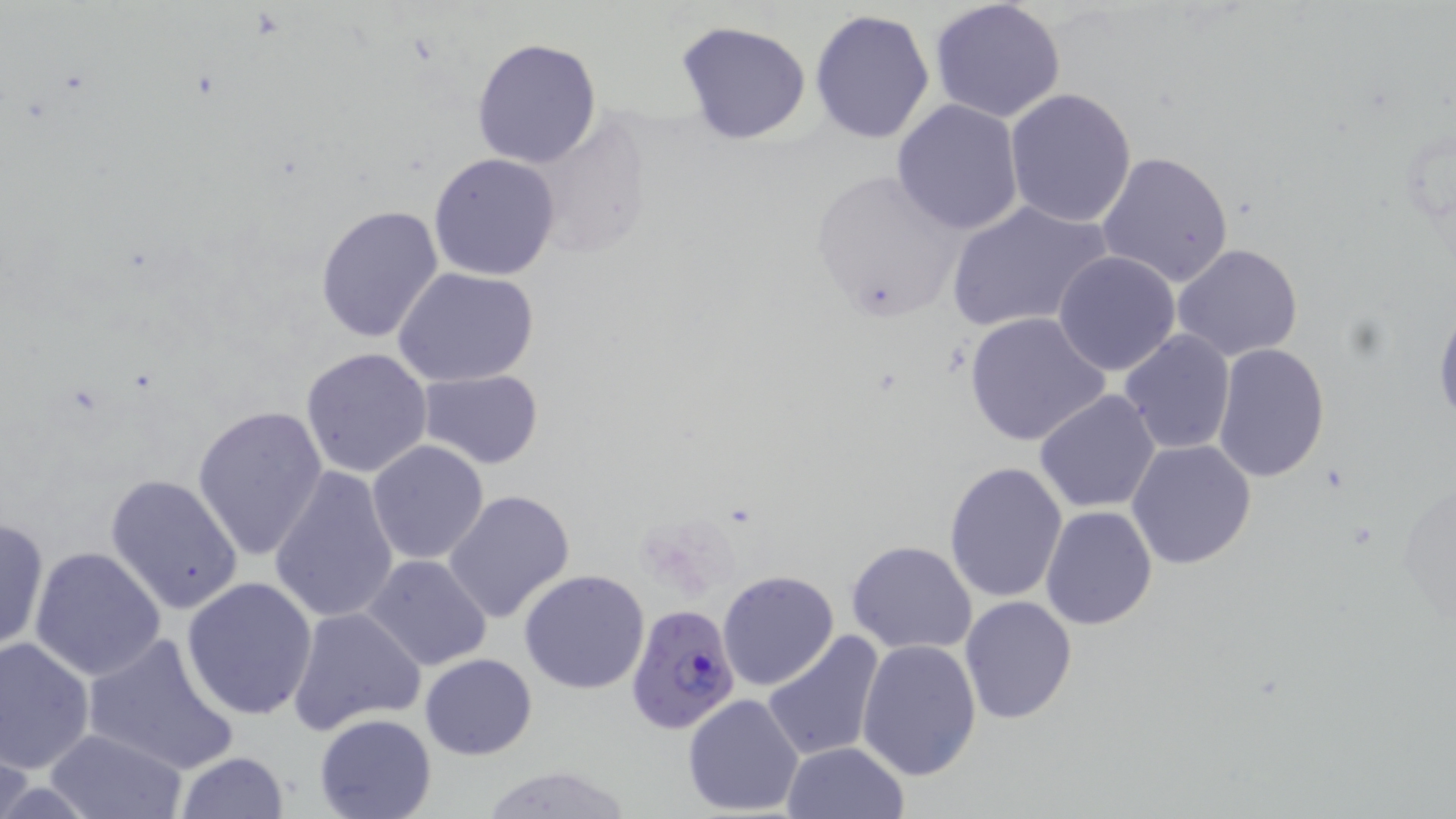 Approximate bounding boxes as (x1,y1)-(x2,y2) corner pairs in pixels. Uninfected red blood cell locations: (929,0)-(1067,123), (808,8)-(936,145), (676,20)-(812,145), (471,38)-(603,168), (1004,89)-(1137,227), (892,99)-(1024,234), (1097,151)-(1237,288), (429,152)-(562,281), (809,166)-(966,320), (946,198)-(1113,335), (315,203)-(444,344), (1172,244)-(1305,363), (1052,251)-(1180,376), (394,267)-(540,387), (1434,299)-(1456,429), (963,311)-(1111,448), (1117,331)-(1235,457), (1211,343)-(1329,484), (301,348)-(433,478), (417,369)-(545,470), (1034,389)-(1162,513), (191,405)-(328,560), (1127,440)-(1257,570), (367,441)-(490,566), (944,461)-(1069,602), (269,465)-(401,627), (105,473)-(244,615), (442,489)-(576,624), (1041,506)-(1157,629), (0,516)-(50,654), (846,539)-(979,655), (29,547)-(167,682), (363,554)-(494,672), (519,569)-(651,694), (719,570)-(838,691), (181,577)-(318,720), (958,594)-(1078,725), (287,607)-(424,734), (82,630)-(240,774), (763,630)-(886,761), (0,635)-(96,775), (857,638)-(982,779), (419,652)-(538,760), (683,693)-(805,817), (313,711)-(437,819), (41,728)-(190,819), (780,741)-(910,819), (172,751)-(289,819), (479,764)-(638,819). Plasmodium falciparum-infected red blood cell locations: (625,604)-(742,735). Slide-level diagnosis: Plasmodium falciparum. May-Grünwald-Giemsa-stained preparation. Thin blood film. Light microscopy. Image is 1456×819 pixels. 1000x magnification. Single field of view.